Classify this cell by malaria status.
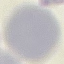

It is uninfected.

preparation: thin smear
image_type: automatically extracted cell patch, resized to 64 × 64 pixels
stain: Giemsa
capture: smartphone through the microscope eyepiece